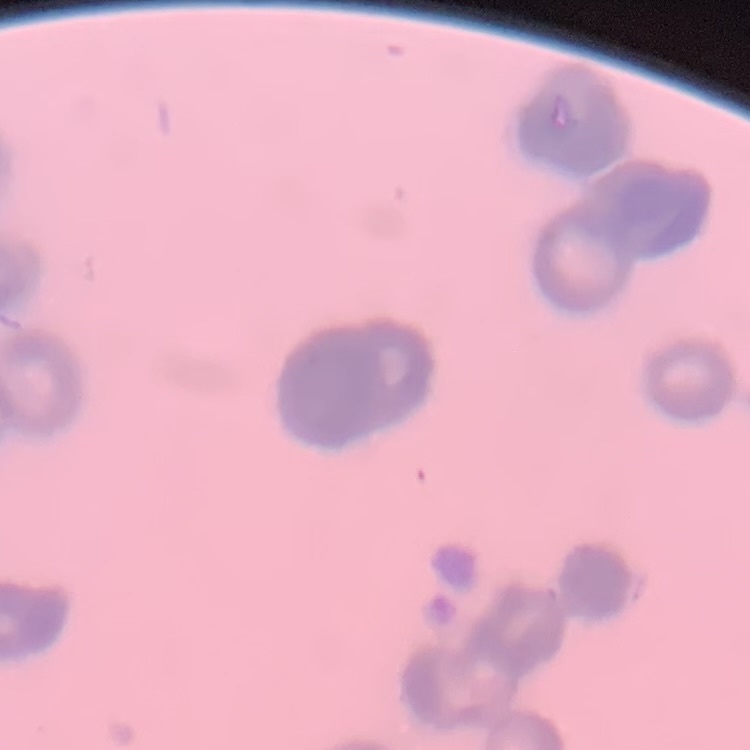

erythrocyte_morphology: rouleaux formation
stain: Field's or Giemsa
preparation: thin blood smear
image_type: square crop of a larger photomicrograph